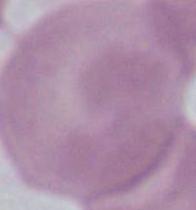

modality = photomicrograph
magnification = 1000x
identification = red blood cell